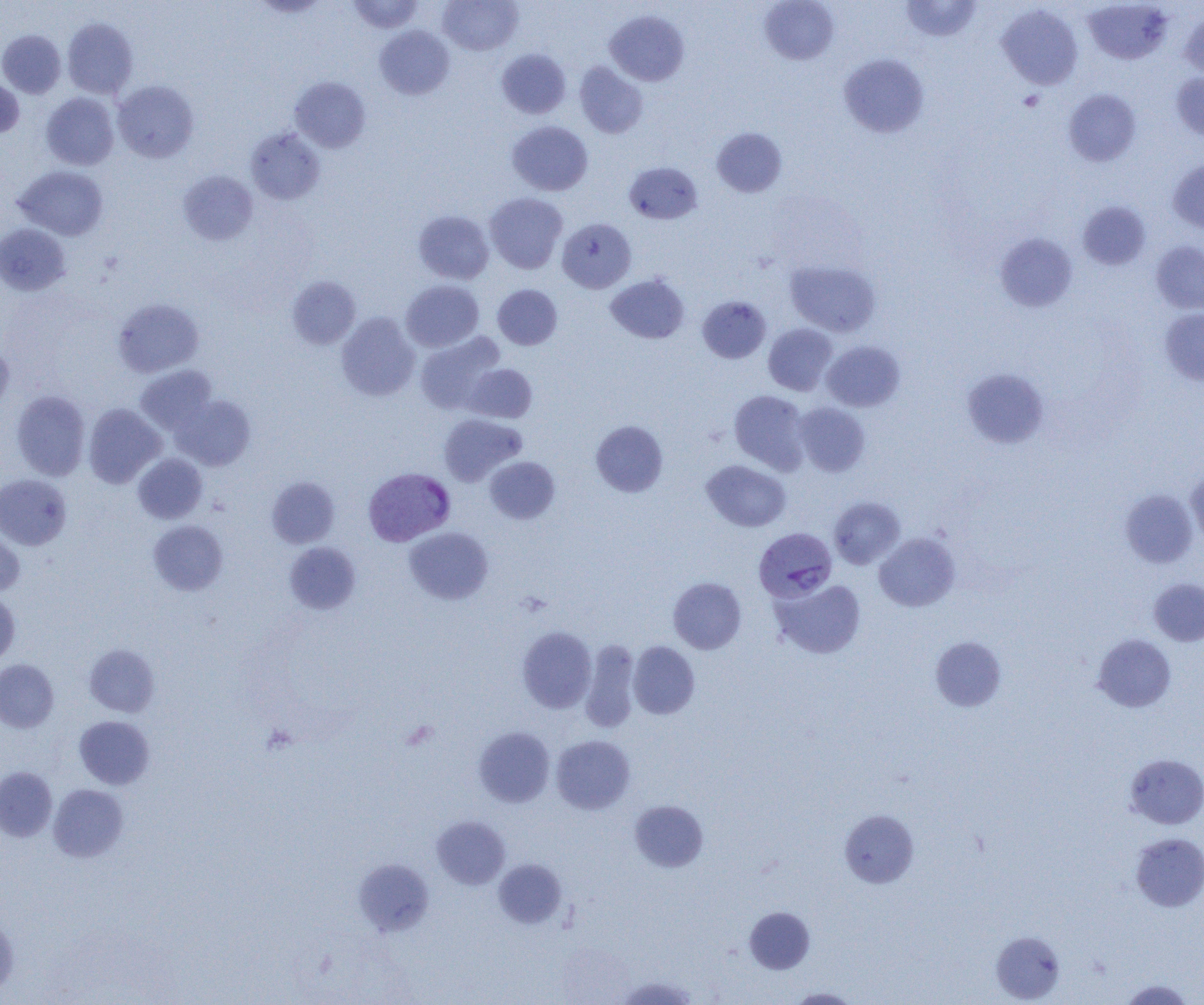

Summary:
  - Coordinate format: approximate bounding boxes as [x1, y1, x2, y2] in pixels
  - Platelet locations: [1018, 90, 1044, 111]
  - Plasmodium vivax-infected red blood cell locations: [363, 467, 455, 545], [753, 527, 836, 602]
  - Uninfected red blood cell locations: [347, 0, 425, 33], [438, 0, 522, 55], [901, 0, 981, 42], [251, 1, 330, 18], [759, 1, 839, 65], [1083, 1, 1173, 64], [997, 5, 1083, 89], [605, 10, 689, 86], [1179, 10, 1204, 79], [63, 17, 138, 98], [374, 25, 454, 100], [0, 30, 66, 98], [497, 49, 571, 118], [838, 53, 929, 138], [574, 62, 648, 139], [1170, 72, 1204, 141], [290, 77, 371, 152], [0, 78, 24, 138], [113, 80, 199, 163], [1063, 89, 1142, 166], [41, 92, 119, 170], [507, 121, 593, 195], [246, 127, 325, 205], [712, 127, 787, 197], [1168, 158, 1204, 233], [624, 162, 702, 224], [14, 166, 110, 240], [178, 171, 258, 245], [484, 193, 568, 274], [1077, 201, 1151, 270], [413, 210, 494, 285], [558, 218, 636, 293], [0, 224, 71, 295], [994, 232, 1078, 312], [1150, 241, 1204, 315], [785, 260, 881, 336], [605, 274, 690, 344], [287, 275, 361, 349], [401, 280, 483, 351], [492, 284, 562, 350], [697, 295, 771, 363], [113, 298, 204, 377], [1160, 308, 1204, 386], [336, 313, 420, 401], [763, 323, 838, 395], [415, 332, 505, 414], [0, 340, 14, 415], [822, 341, 904, 412], [465, 364, 537, 423], [135, 365, 217, 434], [961, 368, 1050, 448], [11, 390, 90, 480], [729, 390, 810, 474], [171, 395, 255, 470], [83, 403, 165, 488], [793, 403, 870, 476], [438, 414, 526, 486], [591, 420, 668, 497], [133, 453, 207, 524], [484, 456, 560, 524], [702, 460, 791, 532], [1186, 468, 1204, 546], [0, 474, 71, 550], [266, 476, 340, 548], [1120, 488, 1198, 568], [828, 496, 905, 569], [148, 520, 228, 596], [0, 525, 25, 597], [404, 527, 493, 604], [874, 532, 960, 612], [284, 542, 361, 614], [668, 577, 747, 654], [771, 578, 866, 659], [1148, 578, 1204, 646], [0, 592, 20, 667], [517, 627, 597, 713], [1092, 633, 1176, 713], [930, 636, 1007, 711], [580, 640, 640, 732], [628, 641, 700, 719], [84, 644, 159, 717], [0, 660, 59, 732], [74, 715, 154, 789], [474, 727, 555, 807], [551, 735, 635, 814], [1125, 753, 1204, 829], [0, 766, 57, 842], [48, 784, 128, 862], [629, 800, 708, 872], [840, 810, 918, 887], [432, 815, 511, 889], [1131, 833, 1204, 912], [354, 859, 434, 936], [494, 859, 567, 928], [744, 907, 815, 974], [0, 913, 19, 997], [991, 931, 1065, 1003], [616, 976, 698, 1005], [1119, 979, 1195, 1004], [785, 987, 861, 1004]
  - Slide-level diagnosis: Plasmodium vivax
  - Field of view: single
  - Magnification: 1000x
  - Image size: 1204×1005 pixels
  - Preparation: thin blood film
  - Modality: optical microscopy